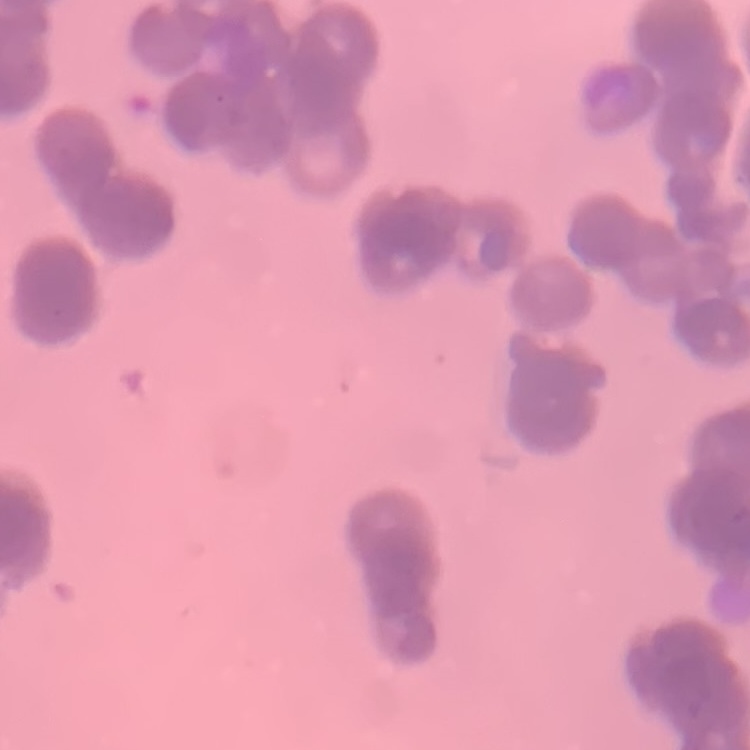
The red blood cells exhibit rouleaux formation. Thin blood smear. Stained with either Field's or Giemsa. One tile cut from a larger photomicrograph.